Comment on the morphology of the erythrocytes.
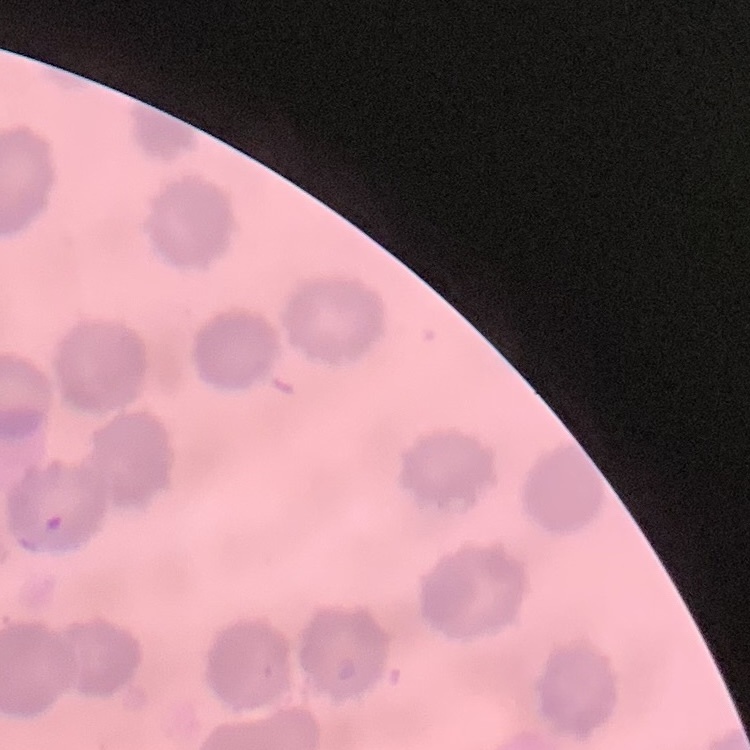

No rouleaux formation.

Summary:
  - Stain: Field's or Giemsa
  - Preparation: thin peripheral smear
  - Image type: one tile cut from a larger photomicrograph